Report the malaria status of this cell.
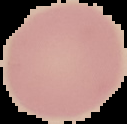
Uninfected.

Summary:
  - Preparation: thin blood smear
  - Image size: 127×124 pixels
  - Image type: cell region segmented out of the field of view; surrounding area masked to black